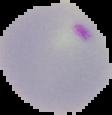

image_size: 112×115 pixels
result: Plasmodium parasites detected
preparation: thin blood smear
image_type: segmented cell region on a black background